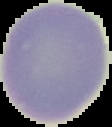

malaria_status: uninfected
image_size: 112×127 pixels
image_type: cell region segmented out of the field of view; surrounding area masked to black
preparation: thin blood film